Give the position of each Plasmodium falciparum parasite with its life-cycle stage, each leukocyte, and any debris.
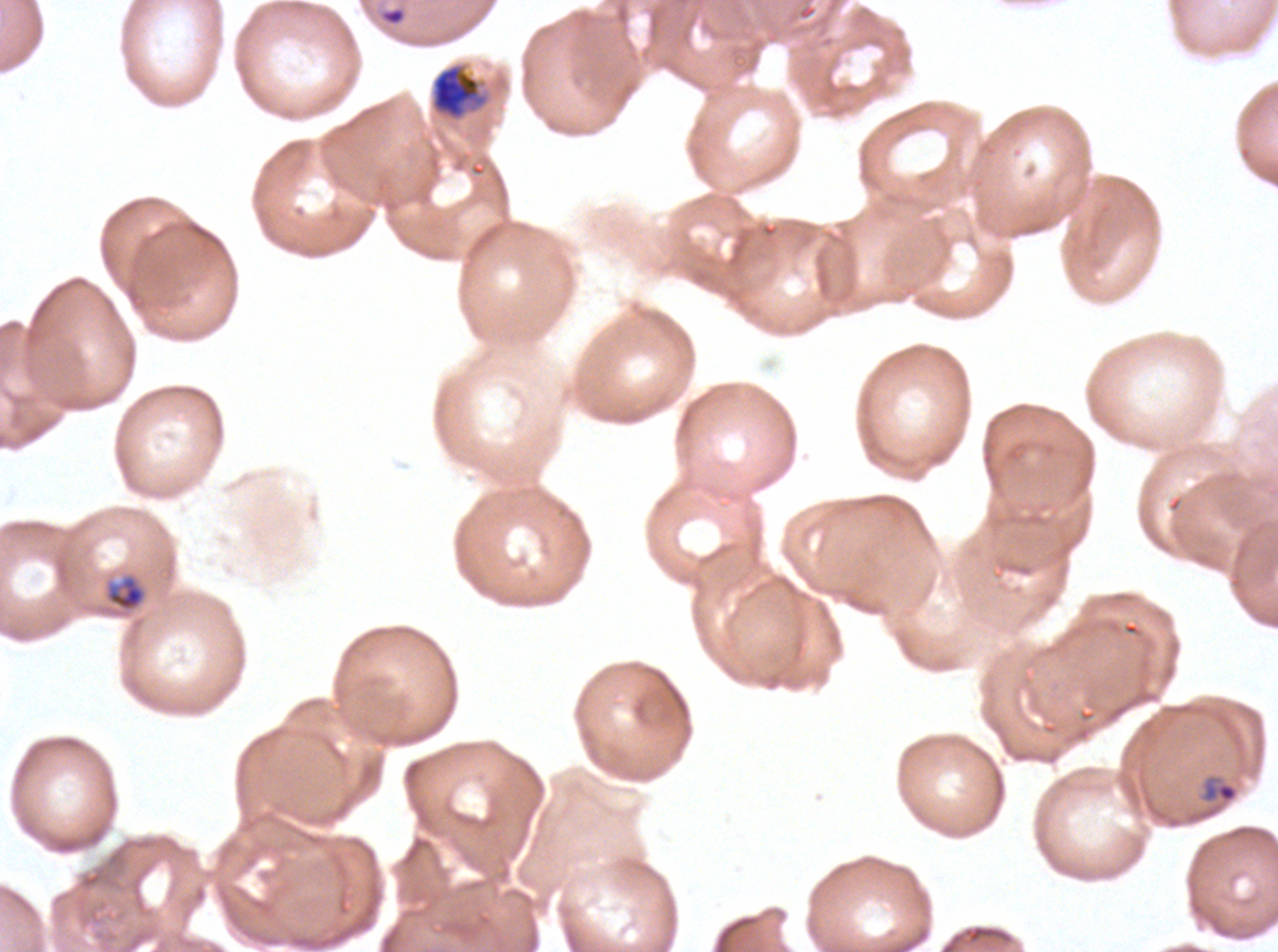

Approximate bounding boxes as (x1, y1, x2, y2) in pixels.
Rings: (378, 6, 408, 27), (1200, 774, 1239, 804).
Late-ring/early-trophozoite forms: (106, 575, 145, 611).
Late trophozoites: (431, 64, 486, 120).
No mid trophozoites, early schizonts, late schizonts, segmenters, gametocytes, leukocytes, or debris observed.

A sub-image separated from a larger composite. Life-cycle stages observed: ring, late-ring/early-trophozoite, late trophozoite. Thin blood smear. Image is 1278×952 pixels. Plasmodium falciparum cultured ex vivo for 24 to 48 hours, from a patient in The Gambia. Giemsa-stained preparation.